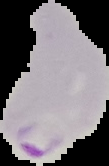
Cell region segmented out of the field of view; the surrounding area is masked to black. Image is 109×166 pixels. From a thin blood smear. Malaria status: parasitized.